Report the malaria status of this cell.
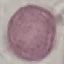
Uninfected.

Thin blood film. Automatically extracted cell patch, resized to 64 × 64 pixels. Giemsa stain. Acquired by smartphone through the microscope eyepiece.